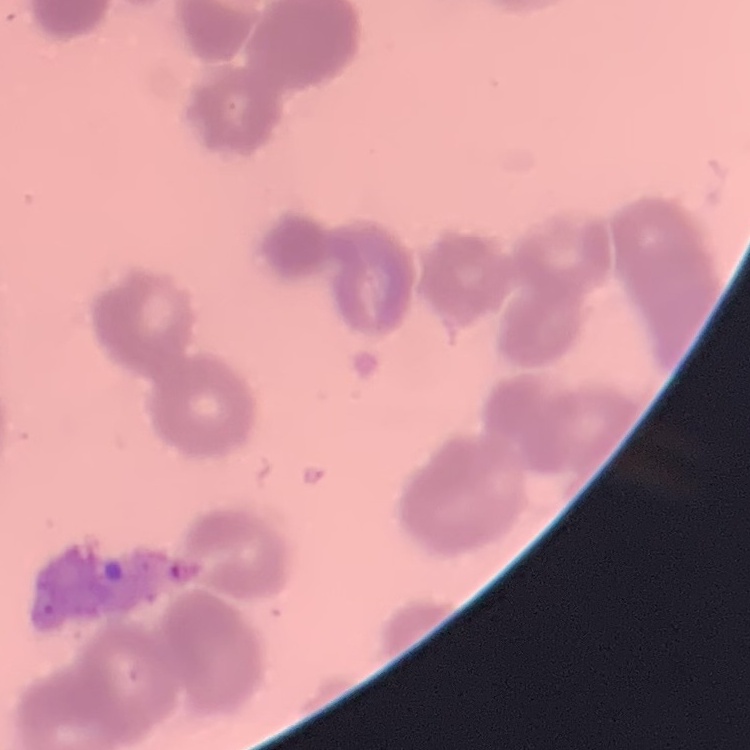
{
  "erythrocyte_morphology": "rouleaux formation",
  "stain": "Field's or Giemsa",
  "preparation": "thin blood smear",
  "image_type": "one tile cut from a larger photomicrograph"
}